Outline Plasmodium malariae parasites and classify them by life-cycle stage.
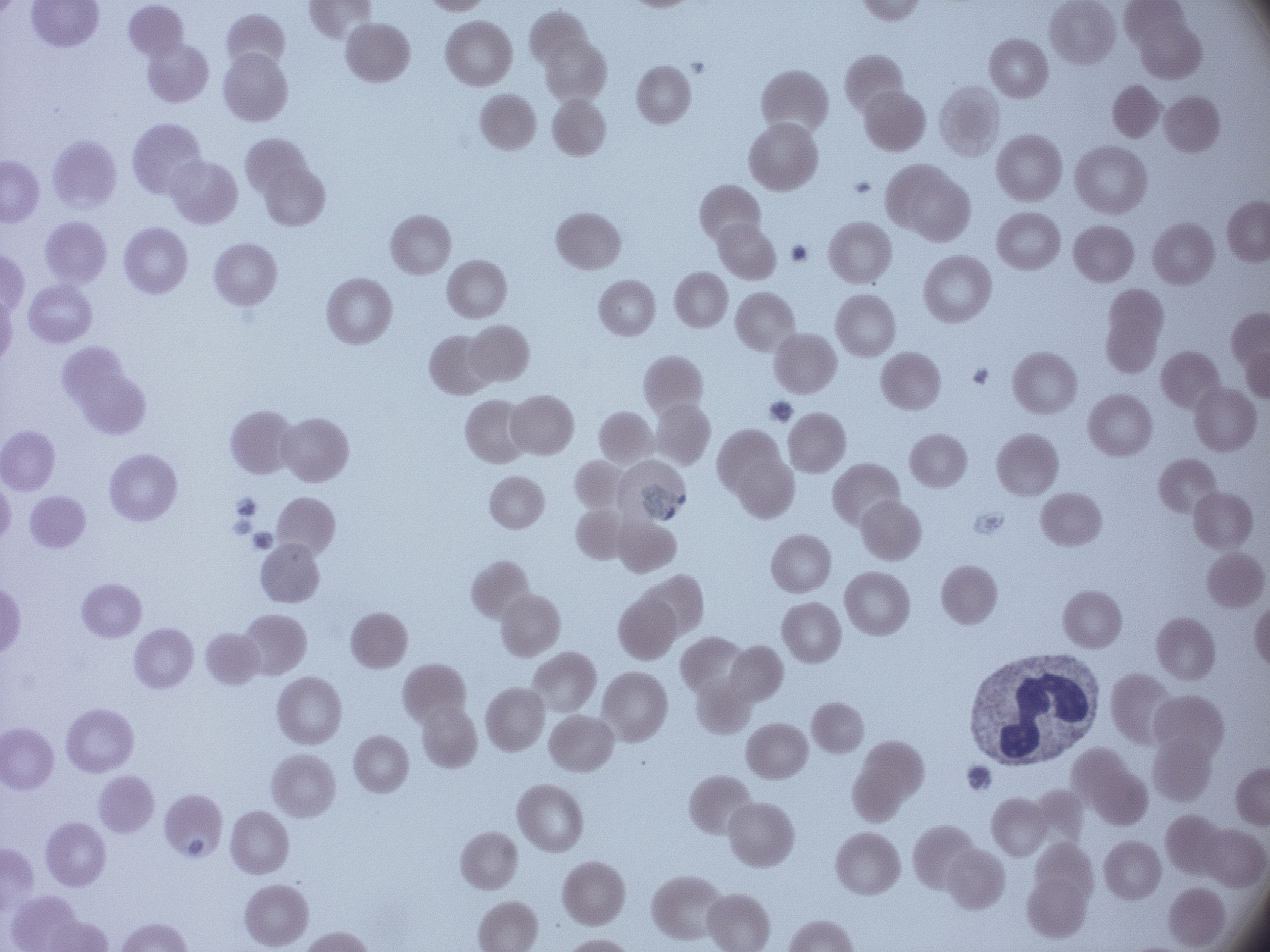

Approximate bounding boxes as [x1, y1, x2, y2] in pixels, from the source annotation, which is not necessarily exhaustive.
Trophozoites: [642, 483, 686, 520].

Species: Plasmodium malariae. Leica DM2000 optical microscope with a built-in camera. Giemsa stain. Image is 1270×952 pixels. Thin blood film. Single field of view. 100x magnification.